Locate every Plasmodium parasite.
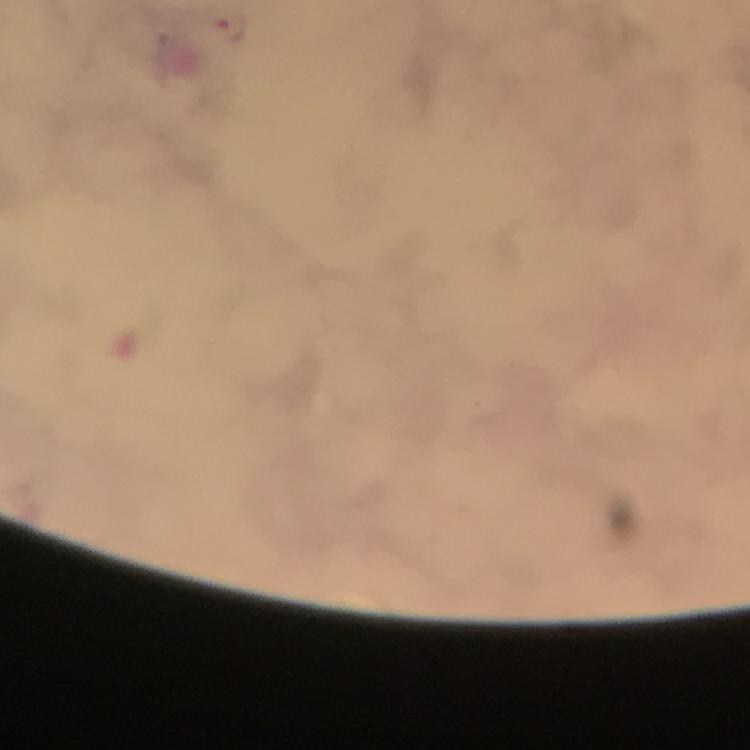

Approximate object centers, in pixels from the top-left corner.
Plasmodium parasites: (x=233, y=26).

preparation = thick blood film
image size = 750×750 pixels
immersion oil = used
context = from a diagnostic examination for malaria
capture = smartphone photograph through a microscope
stain = Giemsa
magnification = 100x
cropped from = a single field of view